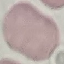

{
  "result": "no malaria parasites detected",
  "stain": "Giemsa",
  "image_type": "automatically extracted cell patch, resized to 64 × 64 pixels",
  "preparation": "thin blood smear",
  "capture": "smartphone through the microscope eyepiece"
}